Report the malaria status of this cell.
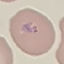

Parasitized.

Giemsa stain. Acquired by smartphone through the microscope eyepiece. Thin smear of blood. Cell patch, automatically extracted from a larger field of view and resized to 64 × 64 pixels.